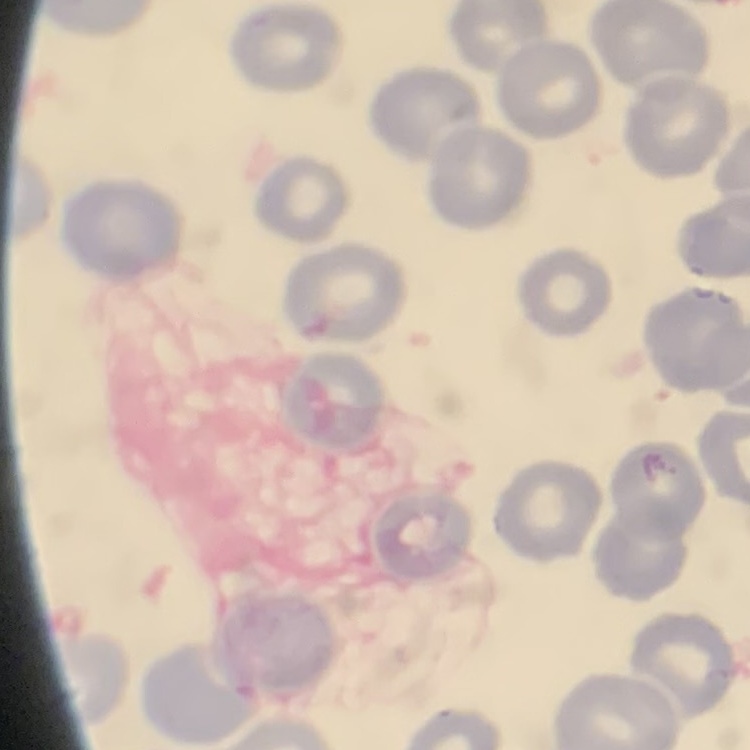
red_blood_cell_morphology: no rouleaux formation
stain: Field's or Giemsa
image_type: square crop of a larger photomicrograph
preparation: thin blood smear